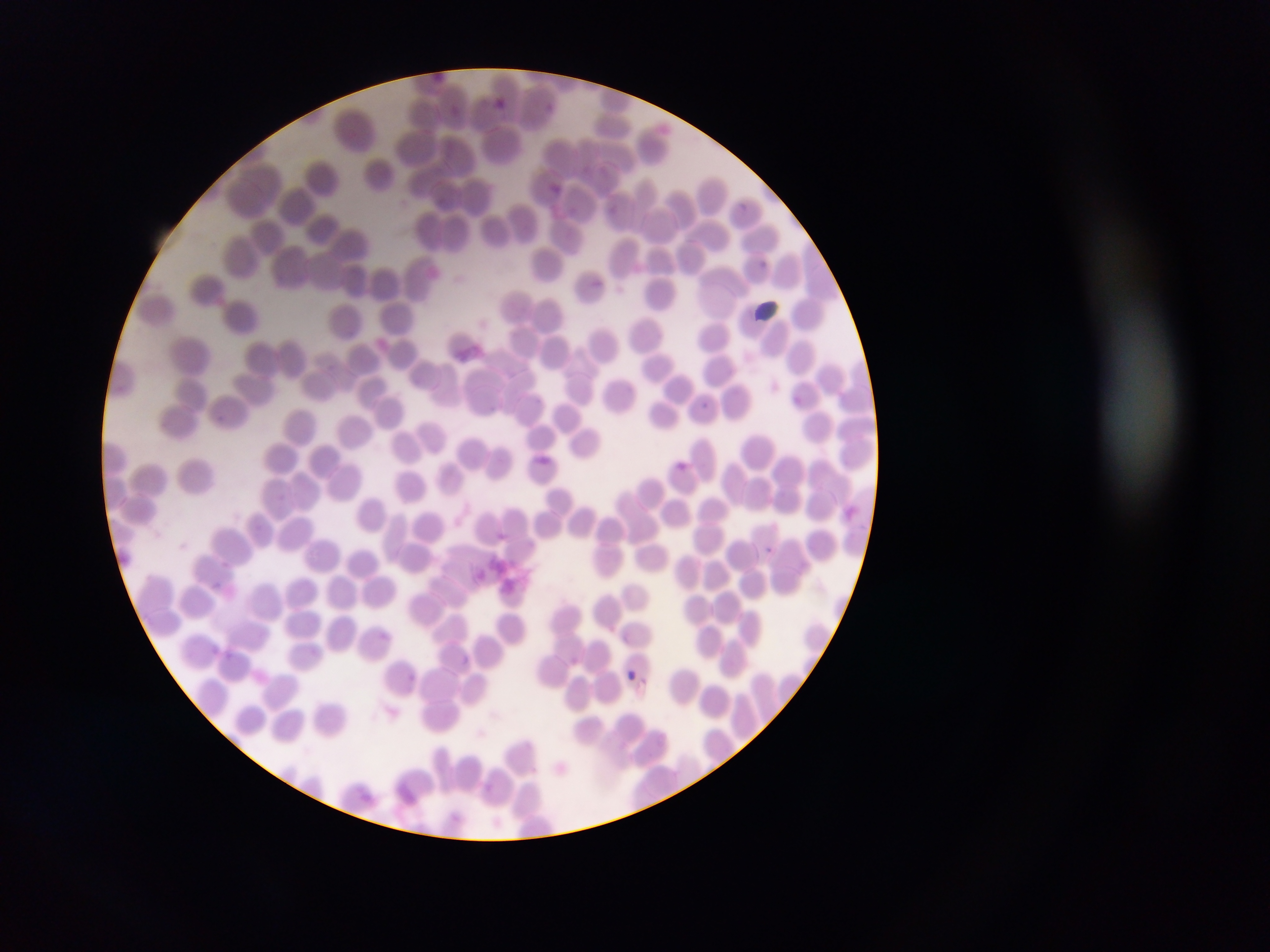

field_of_view: single
preparation: thin blood smear
malaria_parasite_locations: 'approximate bounding boxes as {left, top, right, bottom} in pixels: {549, 182, 576, 197}, {786, 394, 805, 411}, {696, 401, 722, 415}, {673, 459, 700, 475}, {758, 543, 770, 550}, {210, 580, 237, 597}, {220, 649, 237, 665}, {622, 667, 640, 684}'
artifact_stain_precipitate_or_debris_locations: 'approximate bounding boxes as {left, top, right, bottom} in pixels: {751, 298, 786, 323}, {457, 339, 484, 359}, {473, 547, 542, 604}'
image_size: 1270×952 pixels
country: Ghana
capture: mobile-phone photograph through a microscope